Classify this cell by malaria status.
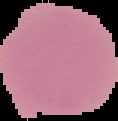
Uninfected.

Summary:
  - Image size: 118×121 pixels
  - Image type: segmented cell region on a black background
  - Preparation: thin blood film